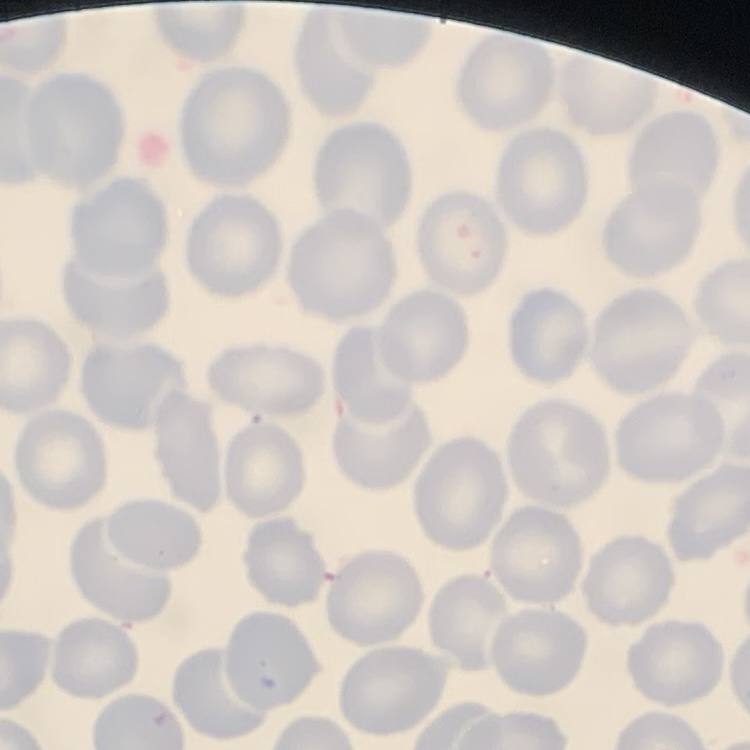
red_blood_cell_morphology: no rouleaux formation
stain: Field's or Giemsa
image_type: one tile cut from a larger photomicrograph
preparation: thin blood smear